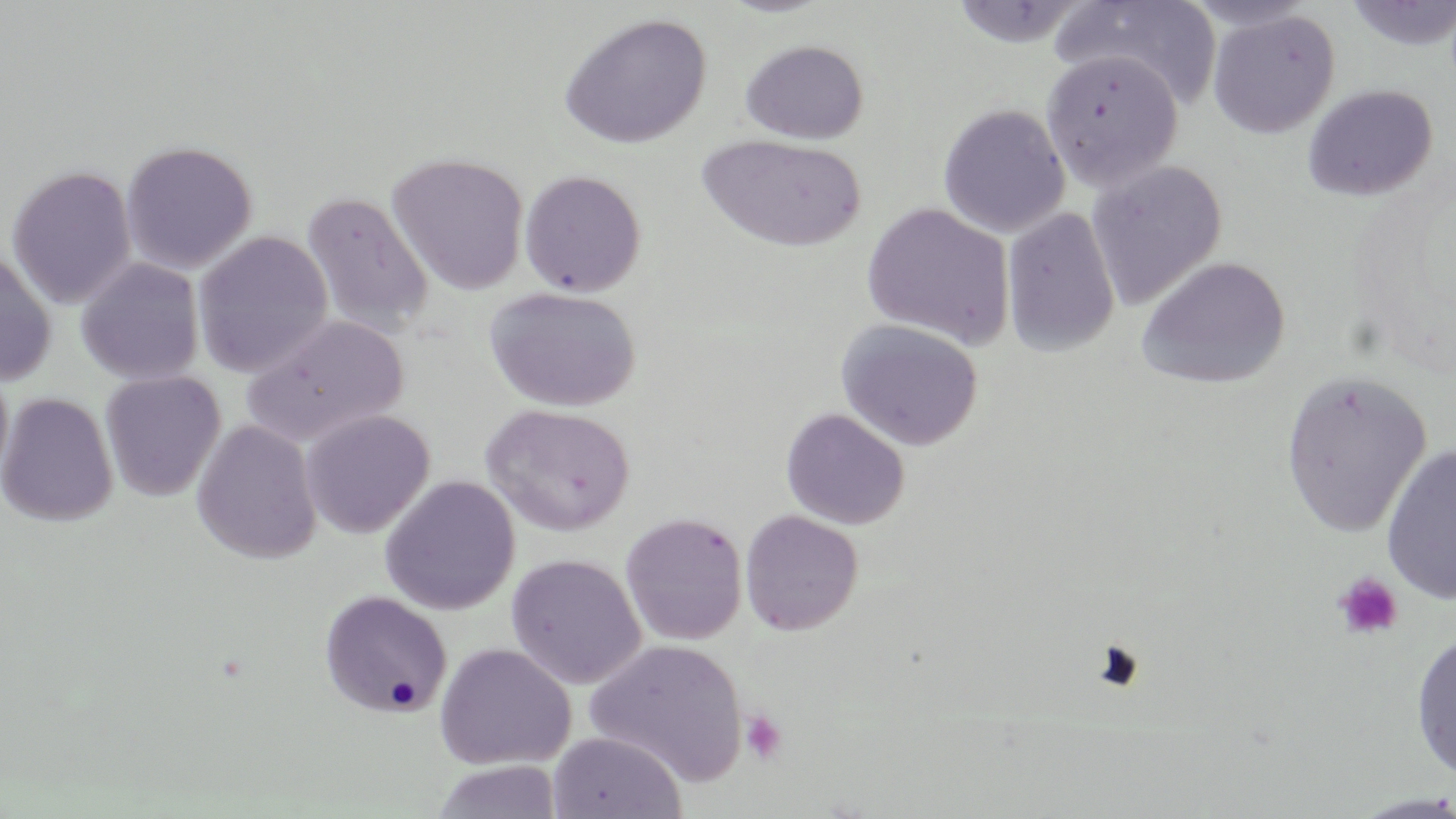

Summary:
  - Coordinate format: approximate bounding boxes as named x1/y1/x2/y2 corners in pixels
  - Platelet locations: (x1=1334, y1=572, x2=1403, y2=640), (x1=740, y1=710, x2=788, y2=765)
  - Uninfected red blood cell locations: (x1=948, y1=0, x2=1088, y2=48), (x1=1052, y1=0, x2=1223, y2=111), (x1=1343, y1=1, x2=1456, y2=52), (x1=1206, y1=9, x2=1341, y2=139), (x1=557, y1=12, x2=712, y2=149), (x1=739, y1=39, x2=869, y2=144), (x1=1040, y1=50, x2=1184, y2=193), (x1=1301, y1=84, x2=1438, y2=201), (x1=937, y1=103, x2=1070, y2=238), (x1=696, y1=132, x2=866, y2=253), (x1=120, y1=140, x2=257, y2=274), (x1=387, y1=152, x2=530, y2=295), (x1=1086, y1=159, x2=1227, y2=311), (x1=6, y1=164, x2=137, y2=309), (x1=519, y1=169, x2=647, y2=297), (x1=300, y1=191, x2=434, y2=338), (x1=861, y1=202, x2=1016, y2=349), (x1=1001, y1=208, x2=1121, y2=359), (x1=193, y1=230, x2=334, y2=378), (x1=0, y1=244, x2=57, y2=385), (x1=1136, y1=256, x2=1290, y2=389), (x1=76, y1=257, x2=204, y2=386), (x1=484, y1=286, x2=643, y2=412), (x1=241, y1=313, x2=409, y2=448), (x1=835, y1=319, x2=984, y2=451), (x1=0, y1=358, x2=14, y2=490), (x1=1279, y1=369, x2=1432, y2=538), (x1=100, y1=370, x2=226, y2=502), (x1=1, y1=392, x2=118, y2=527), (x1=481, y1=403, x2=636, y2=537), (x1=780, y1=408, x2=910, y2=530), (x1=301, y1=410, x2=435, y2=538), (x1=191, y1=419, x2=322, y2=565), (x1=1380, y1=444, x2=1456, y2=605), (x1=379, y1=475, x2=521, y2=615), (x1=740, y1=509, x2=863, y2=636), (x1=620, y1=512, x2=748, y2=646), (x1=505, y1=553, x2=647, y2=689), (x1=319, y1=590, x2=452, y2=719), (x1=1410, y1=629, x2=1456, y2=782), (x1=584, y1=638, x2=748, y2=787), (x1=434, y1=642, x2=576, y2=770), (x1=547, y1=731, x2=687, y2=818), (x1=432, y1=760, x2=563, y2=818), (x1=1345, y1=792, x2=1456, y2=818)
  - Slide-level diagnosis: negative for blood parasites
  - Field of view: one of a larger specimen
  - Stain: May-Grünwald-Giemsa
  - Image size: 1456×819 pixels
  - Preparation: thin blood smear
  - Magnification: 1000x
  - Modality: light microscopy